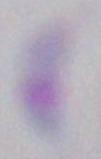
identification = Toxoplasma gondii
modality = micrograph
magnification = 1000x